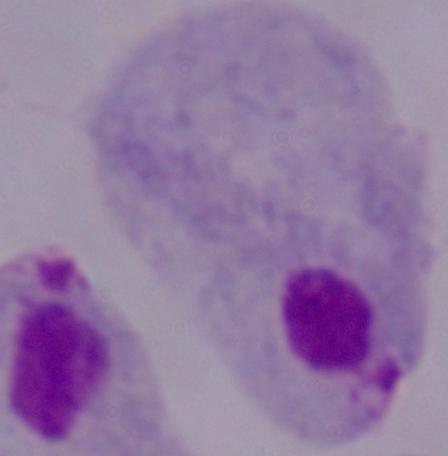
{
  "identification": "trichomonad",
  "magnification": "1000x",
  "modality": "micrograph"
}